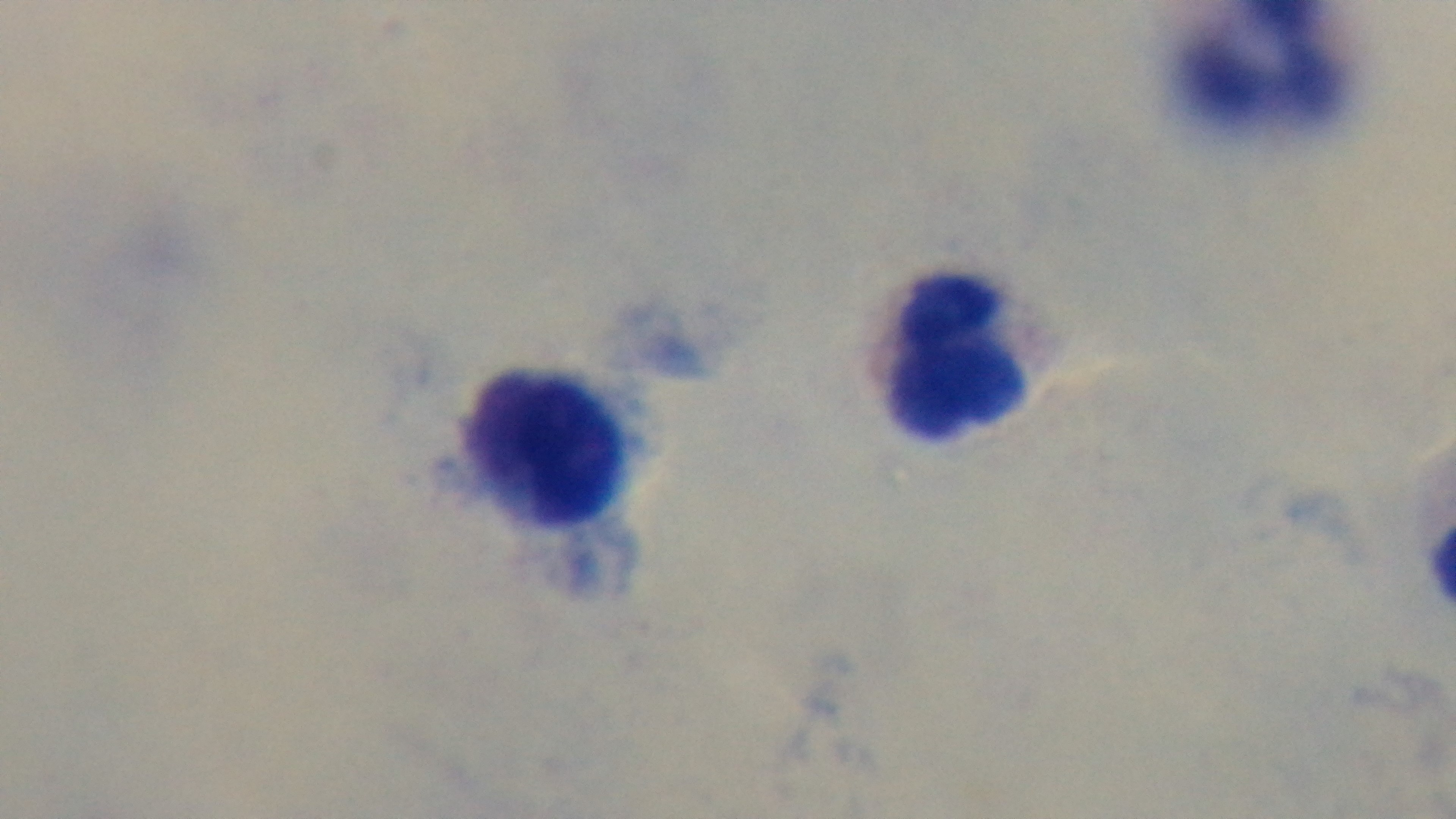
Photomicrograph. One field from the slide. Oil-immersion objective, 100x. Giemsa stain. Malaria status: uninfected. Captured with a mounted 4K digital camera. Preparation: thick blood film.